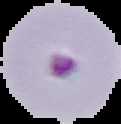

Malaria status: parasitized. From a thin blood smear. Segmented cell region on a black background. Image is 121×124 pixels.